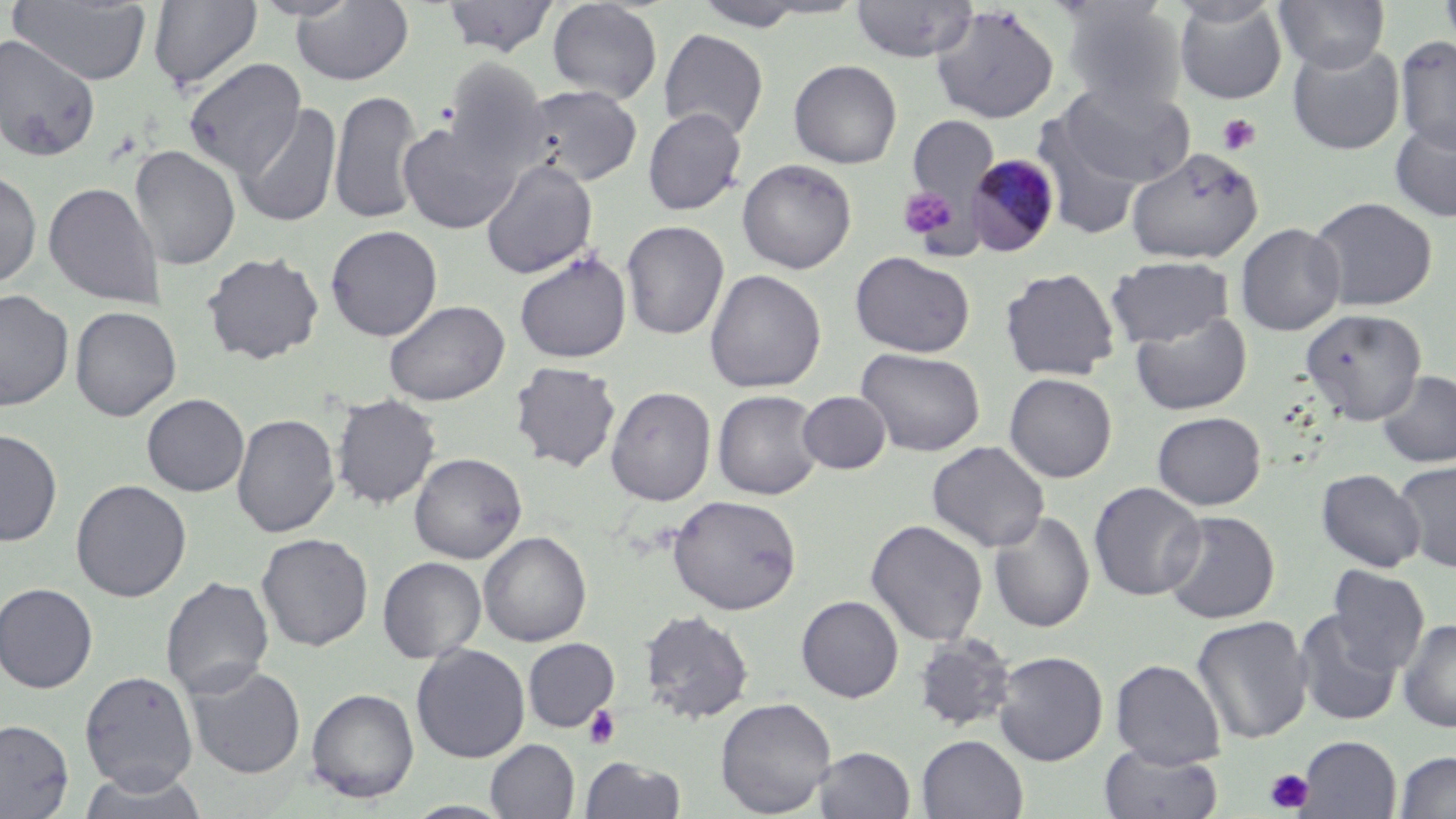

slide-level diagnosis = Plasmodium malariae
image size = 1456×819 pixels
platelet locations = approximate bounding boxes as (x1, y1, x2, y2) in pixels: (1217, 113, 1261, 156), (899, 185, 959, 244), (583, 705, 621, 750), (1265, 768, 1314, 813)
modality = light microscopy
uninfected red blood cell locations = approximate bounding boxes as (x1, y1, x2, y2) in pixels: (248, 0, 363, 21), (440, 0, 560, 58), (850, 0, 978, 62), (1174, 0, 1287, 104), (1275, 0, 1389, 73), (1438, 0, 1456, 52), (7, 1, 153, 85), (148, 1, 263, 93), (291, 1, 414, 86), (547, 1, 663, 104), (692, 1, 814, 31), (1059, 3, 1186, 113), (929, 5, 1060, 124), (659, 28, 769, 140), (0, 34, 102, 163), (1395, 34, 1456, 153), (1287, 40, 1405, 155), (183, 57, 306, 179), (441, 57, 552, 181), (788, 60, 902, 168), (1056, 79, 1195, 188), (517, 84, 643, 187), (329, 89, 423, 225), (235, 103, 342, 228), (642, 108, 747, 215), (1032, 113, 1150, 238), (907, 115, 999, 210), (1389, 118, 1456, 223), (396, 119, 521, 234), (129, 145, 240, 270), (1125, 147, 1263, 264), (737, 158, 857, 274), (480, 159, 599, 279), (0, 169, 42, 288), (43, 182, 165, 308), (1308, 196, 1437, 311), (620, 220, 729, 340), (1235, 222, 1346, 335), (325, 225, 443, 341), (514, 250, 633, 363), (202, 251, 325, 364), (849, 251, 975, 357), (1106, 256, 1234, 348), (999, 266, 1120, 380), (705, 269, 826, 394), (0, 289, 74, 411), (384, 299, 509, 406), (70, 306, 181, 421), (1300, 308, 1427, 425), (1131, 311, 1251, 415), (856, 347, 985, 456), (510, 361, 622, 472), (1377, 370, 1456, 468), (1004, 372, 1117, 483), (605, 386, 716, 506), (712, 389, 824, 500), (798, 391, 891, 474), (331, 392, 441, 509), (141, 393, 249, 496), (1151, 411, 1266, 510), (232, 413, 341, 538), (0, 428, 62, 547), (926, 440, 1050, 552), (409, 452, 526, 563), (1394, 460, 1456, 572), (1316, 468, 1425, 572), (70, 479, 192, 602), (1088, 482, 1206, 601), (667, 494, 802, 615), (988, 510, 1095, 633), (1161, 510, 1280, 624), (865, 518, 988, 647), (478, 530, 591, 647), (256, 532, 374, 651), (377, 556, 487, 663), (1326, 565, 1430, 674), (160, 576, 274, 699), (0, 582, 98, 693), (796, 595, 904, 702), (639, 609, 754, 724), (1294, 609, 1403, 726), (1191, 615, 1312, 744), (1397, 618, 1456, 732), (913, 633, 1016, 733), (523, 637, 620, 732), (411, 643, 530, 763), (993, 650, 1108, 766), (1111, 658, 1226, 768), (185, 663, 306, 779), (79, 670, 199, 793), (306, 688, 420, 802), (716, 697, 836, 817), (0, 718, 74, 818), (916, 735, 1028, 818), (1297, 735, 1401, 819), (486, 739, 579, 818), (1099, 744, 1223, 819), (813, 746, 915, 818), (1394, 751, 1456, 817), (580, 756, 687, 818), (77, 767, 210, 819), (403, 800, 516, 818)
stain = May-Grünwald-Giemsa
magnification = 1000x
Plasmodium malariae-infected red blood cell locations = approximate bounding boxes as (x1, y1, x2, y2) in pixels: (965, 153, 1062, 257)
field of view = one of a larger specimen
preparation = thin blood smear